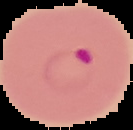

Summary:
  - Preparation: thin blood film
  - Image size: 133×130 pixels
  - Image type: segmented cell region with the area outside set to black
  - Result: Plasmodium parasites detected